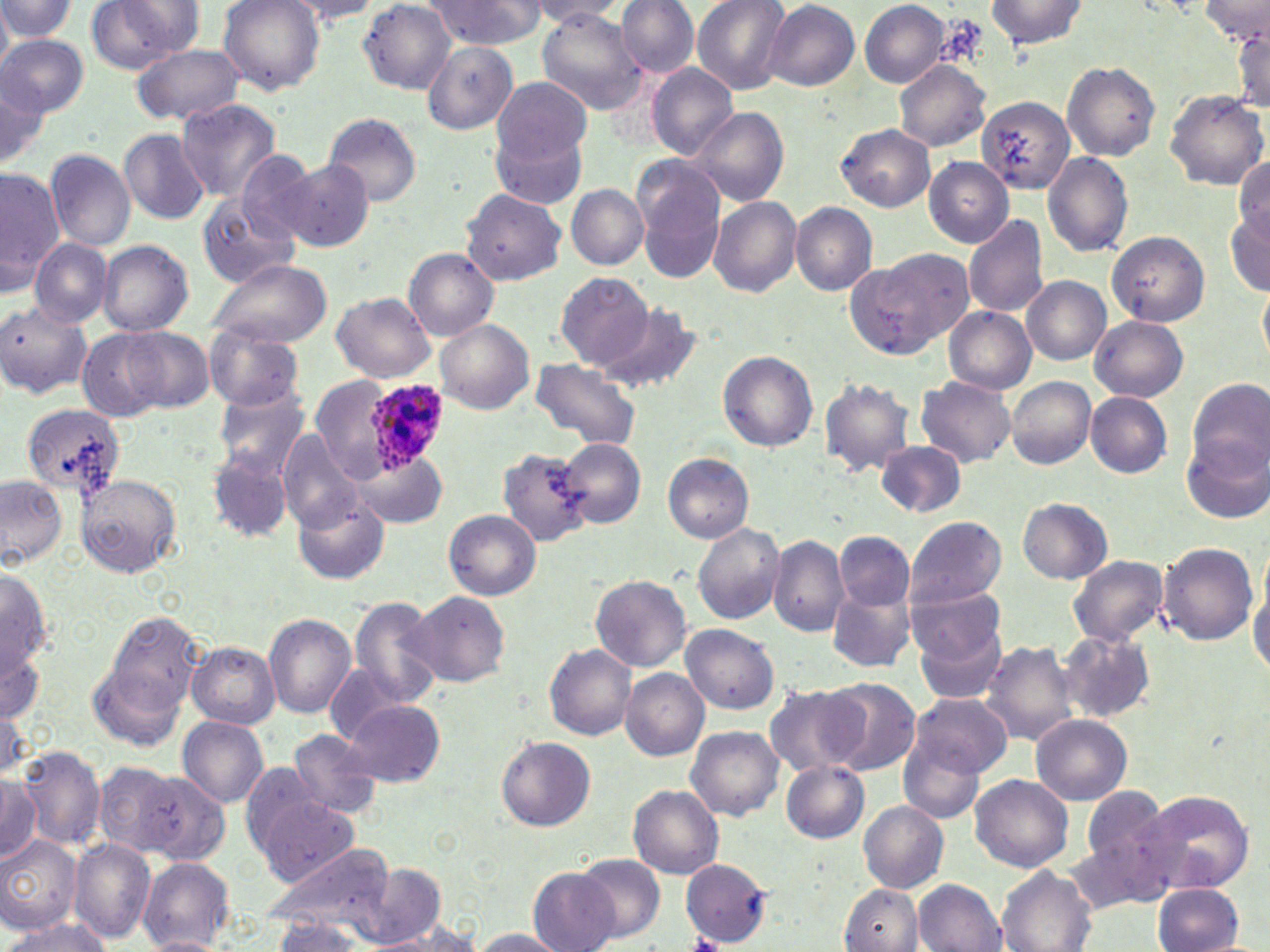
Approximate bounding boxes as named x1/y1/x2/y2 corners in pixels. Uninfected red blood cell locations: (x1=219, y1=0, x2=324, y2=94), (x1=426, y1=0, x2=547, y2=49), (x1=617, y1=0, x2=699, y2=78), (x1=690, y1=0, x2=791, y2=94), (x1=986, y1=0, x2=1087, y2=50), (x1=0, y1=1, x2=79, y2=42), (x1=86, y1=1, x2=198, y2=72), (x1=282, y1=1, x2=384, y2=25), (x1=361, y1=1, x2=456, y2=94), (x1=530, y1=1, x2=629, y2=23), (x1=859, y1=1, x2=948, y2=86), (x1=1201, y1=1, x2=1268, y2=46), (x1=765, y1=2, x2=859, y2=90), (x1=0, y1=5, x2=12, y2=74), (x1=537, y1=10, x2=649, y2=115), (x1=1229, y1=25, x2=1270, y2=114), (x1=0, y1=34, x2=88, y2=116), (x1=423, y1=42, x2=516, y2=134), (x1=133, y1=43, x2=243, y2=126), (x1=143, y1=55, x2=264, y2=170), (x1=895, y1=61, x2=990, y2=151), (x1=1061, y1=61, x2=1161, y2=160), (x1=645, y1=64, x2=736, y2=160), (x1=0, y1=74, x2=48, y2=168), (x1=492, y1=75, x2=592, y2=165), (x1=1164, y1=90, x2=1269, y2=190), (x1=976, y1=95, x2=1070, y2=194), (x1=177, y1=99, x2=283, y2=203), (x1=690, y1=107, x2=789, y2=206), (x1=324, y1=113, x2=422, y2=207), (x1=837, y1=124, x2=934, y2=211), (x1=120, y1=128, x2=212, y2=225), (x1=494, y1=128, x2=587, y2=211), (x1=45, y1=150, x2=135, y2=250), (x1=236, y1=150, x2=320, y2=244), (x1=1042, y1=151, x2=1132, y2=257), (x1=1233, y1=156, x2=1270, y2=244), (x1=634, y1=157, x2=727, y2=280), (x1=925, y1=157, x2=1013, y2=246), (x1=281, y1=158, x2=374, y2=252), (x1=0, y1=166, x2=62, y2=293), (x1=567, y1=184, x2=648, y2=269), (x1=461, y1=188, x2=567, y2=286), (x1=197, y1=194, x2=295, y2=287), (x1=709, y1=197, x2=801, y2=296), (x1=791, y1=202, x2=877, y2=294), (x1=1226, y1=208, x2=1270, y2=294), (x1=964, y1=214, x2=1049, y2=317), (x1=1107, y1=231, x2=1209, y2=326), (x1=29, y1=237, x2=113, y2=328), (x1=98, y1=240, x2=194, y2=335), (x1=404, y1=249, x2=498, y2=339), (x1=849, y1=249, x2=969, y2=357), (x1=209, y1=259, x2=332, y2=347), (x1=557, y1=271, x2=654, y2=370), (x1=1022, y1=275, x2=1111, y2=365), (x1=1258, y1=285, x2=1270, y2=366), (x1=332, y1=291, x2=435, y2=383), (x1=1, y1=303, x2=91, y2=398), (x1=596, y1=305, x2=701, y2=396), (x1=944, y1=307, x2=1035, y2=393), (x1=1091, y1=315, x2=1188, y2=401), (x1=436, y1=320, x2=532, y2=413), (x1=121, y1=325, x2=213, y2=412), (x1=204, y1=325, x2=302, y2=410), (x1=77, y1=329, x2=165, y2=420), (x1=718, y1=351, x2=819, y2=451), (x1=530, y1=357, x2=641, y2=450), (x1=310, y1=376, x2=387, y2=483), (x1=1006, y1=376, x2=1097, y2=468), (x1=818, y1=377, x2=915, y2=476), (x1=914, y1=377, x2=1016, y2=467), (x1=1187, y1=377, x2=1268, y2=476), (x1=214, y1=385, x2=310, y2=476), (x1=1085, y1=392, x2=1173, y2=478), (x1=22, y1=404, x2=127, y2=496), (x1=278, y1=433, x2=367, y2=533), (x1=1183, y1=435, x2=1270, y2=527), (x1=559, y1=438, x2=646, y2=529), (x1=875, y1=442, x2=967, y2=518), (x1=497, y1=447, x2=593, y2=547), (x1=206, y1=451, x2=293, y2=544), (x1=352, y1=451, x2=447, y2=527), (x1=664, y1=454, x2=753, y2=542), (x1=76, y1=474, x2=180, y2=578), (x1=0, y1=476, x2=67, y2=566), (x1=295, y1=495, x2=389, y2=586), (x1=1018, y1=499, x2=1111, y2=582), (x1=444, y1=509, x2=541, y2=600), (x1=903, y1=515, x2=1006, y2=610), (x1=692, y1=522, x2=785, y2=626), (x1=836, y1=532, x2=914, y2=611), (x1=768, y1=536, x2=850, y2=637), (x1=1156, y1=542, x2=1259, y2=646), (x1=1067, y1=555, x2=1168, y2=647), (x1=1, y1=567, x2=54, y2=686), (x1=591, y1=574, x2=692, y2=672), (x1=1248, y1=577, x2=1270, y2=680), (x1=905, y1=583, x2=1006, y2=670), (x1=826, y1=590, x2=917, y2=673), (x1=410, y1=592, x2=509, y2=687), (x1=346, y1=597, x2=443, y2=706), (x1=98, y1=609, x2=207, y2=732), (x1=264, y1=612, x2=356, y2=720), (x1=912, y1=614, x2=1008, y2=708), (x1=681, y1=625, x2=780, y2=714), (x1=1055, y1=630, x2=1156, y2=724), (x1=0, y1=640, x2=43, y2=728), (x1=980, y1=641, x2=1080, y2=747), (x1=188, y1=643, x2=278, y2=727), (x1=546, y1=645, x2=637, y2=739), (x1=89, y1=662, x2=184, y2=752), (x1=326, y1=666, x2=413, y2=744), (x1=620, y1=670, x2=709, y2=759), (x1=824, y1=679, x2=920, y2=775), (x1=764, y1=684, x2=866, y2=777), (x1=906, y1=692, x2=1012, y2=779), (x1=345, y1=700, x2=445, y2=787), (x1=1031, y1=714, x2=1133, y2=804), (x1=177, y1=715, x2=269, y2=808), (x1=685, y1=726, x2=783, y2=819), (x1=287, y1=728, x2=384, y2=819), (x1=897, y1=736, x2=985, y2=823), (x1=498, y1=737, x2=594, y2=831), (x1=18, y1=744, x2=104, y2=850), (x1=94, y1=758, x2=180, y2=857), (x1=240, y1=760, x2=326, y2=858), (x1=780, y1=760, x2=870, y2=842), (x1=124, y1=767, x2=232, y2=866), (x1=0, y1=774, x2=41, y2=864), (x1=970, y1=774, x2=1074, y2=872), (x1=629, y1=785, x2=722, y2=878), (x1=1075, y1=786, x2=1178, y2=895), (x1=1140, y1=789, x2=1255, y2=895), (x1=259, y1=797, x2=359, y2=886), (x1=858, y1=801, x2=949, y2=892), (x1=0, y1=834, x2=81, y2=932), (x1=69, y1=840, x2=156, y2=944), (x1=263, y1=840, x2=395, y2=939), (x1=575, y1=853, x2=665, y2=943), (x1=138, y1=858, x2=234, y2=950), (x1=679, y1=859, x2=772, y2=944), (x1=356, y1=866, x2=449, y2=948), (x1=997, y1=868, x2=1096, y2=952), (x1=529, y1=869, x2=619, y2=952), (x1=913, y1=879, x2=1007, y2=951), (x1=838, y1=884, x2=922, y2=952), (x1=1155, y1=884, x2=1244, y2=951), (x1=0, y1=917, x2=113, y2=952), (x1=272, y1=918, x2=372, y2=951), (x1=362, y1=928, x2=482, y2=951), (x1=470, y1=928, x2=566, y2=951), (x1=140, y1=935, x2=225, y2=951). Plasmodium ovale-infected red blood cell locations: (x1=368, y1=380, x2=449, y2=476). Slide-level diagnosis: Plasmodium ovale. Light microscopy. May-Grünwald-Giemsa-stained preparation. 1000x magnification. Thin blood film. Single field of view. Image is 1270×952 pixels.